Describe the morphology of the red blood cells.
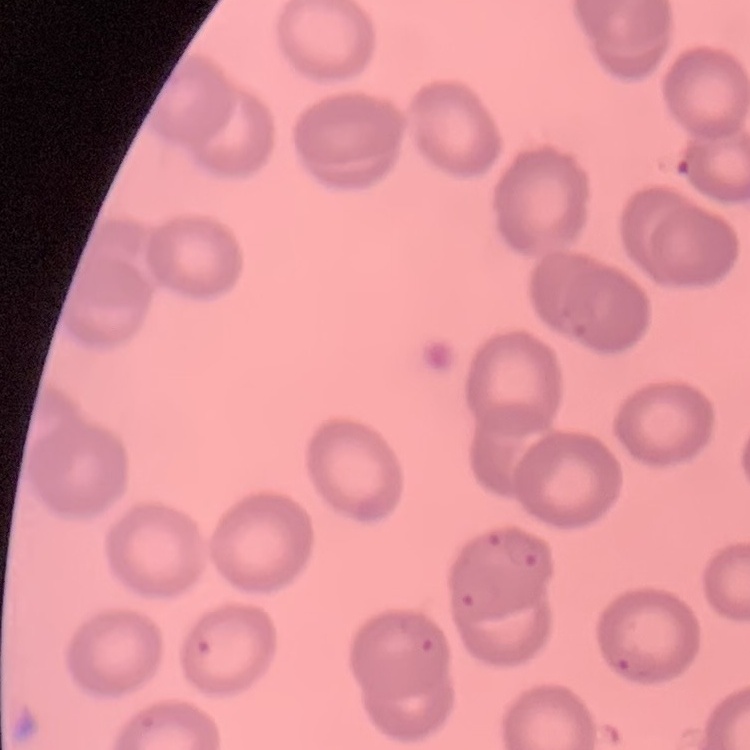

They show no rouleaux formation.

stain = Field's or Giemsa
preparation = thin blood smear
image type = one tile cut from a larger photomicrograph